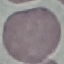
Result: negative for malaria parasites. Thin blood smear. Giemsa stain. Photographed with a smartphone camera at the microscope eyepiece. Automatically extracted cell patch, resized to 64 × 64 pixels.